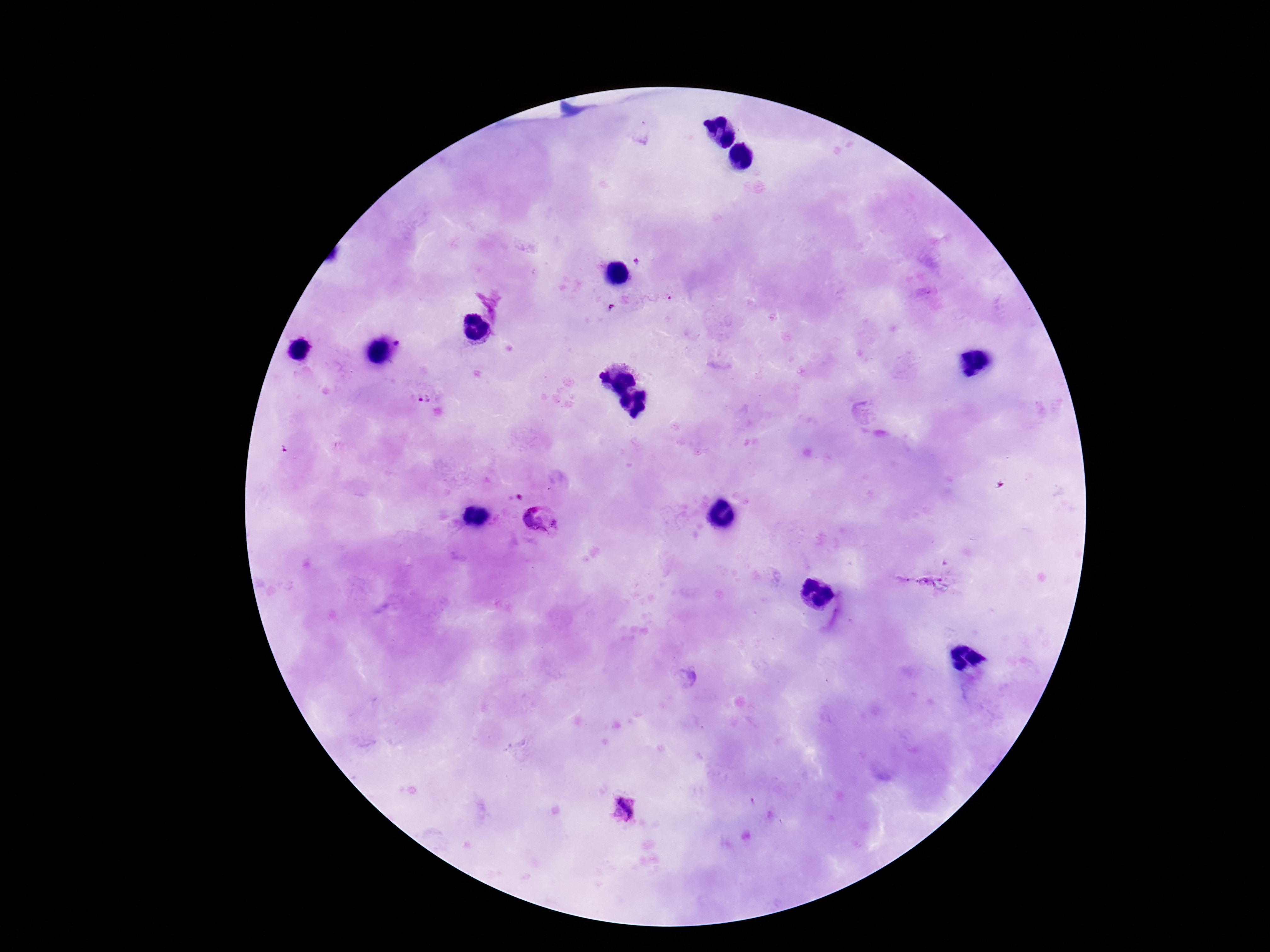 Approximate centers as (x, y) in pixels. Plasmodium parasite locations: (400, 342), (423, 399), (542, 521), (624, 809). Thick peripheral-blood smear. Smartphone photograph taken through the microscope eyepiece. 100x magnification. Image is 1270×952 pixels. One field from this slide. Giemsa stain. Patient malaria status: infected.